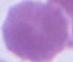
Summary:
  - Modality: micrograph
  - Identification: erythrocyte
  - Magnification: 1000x